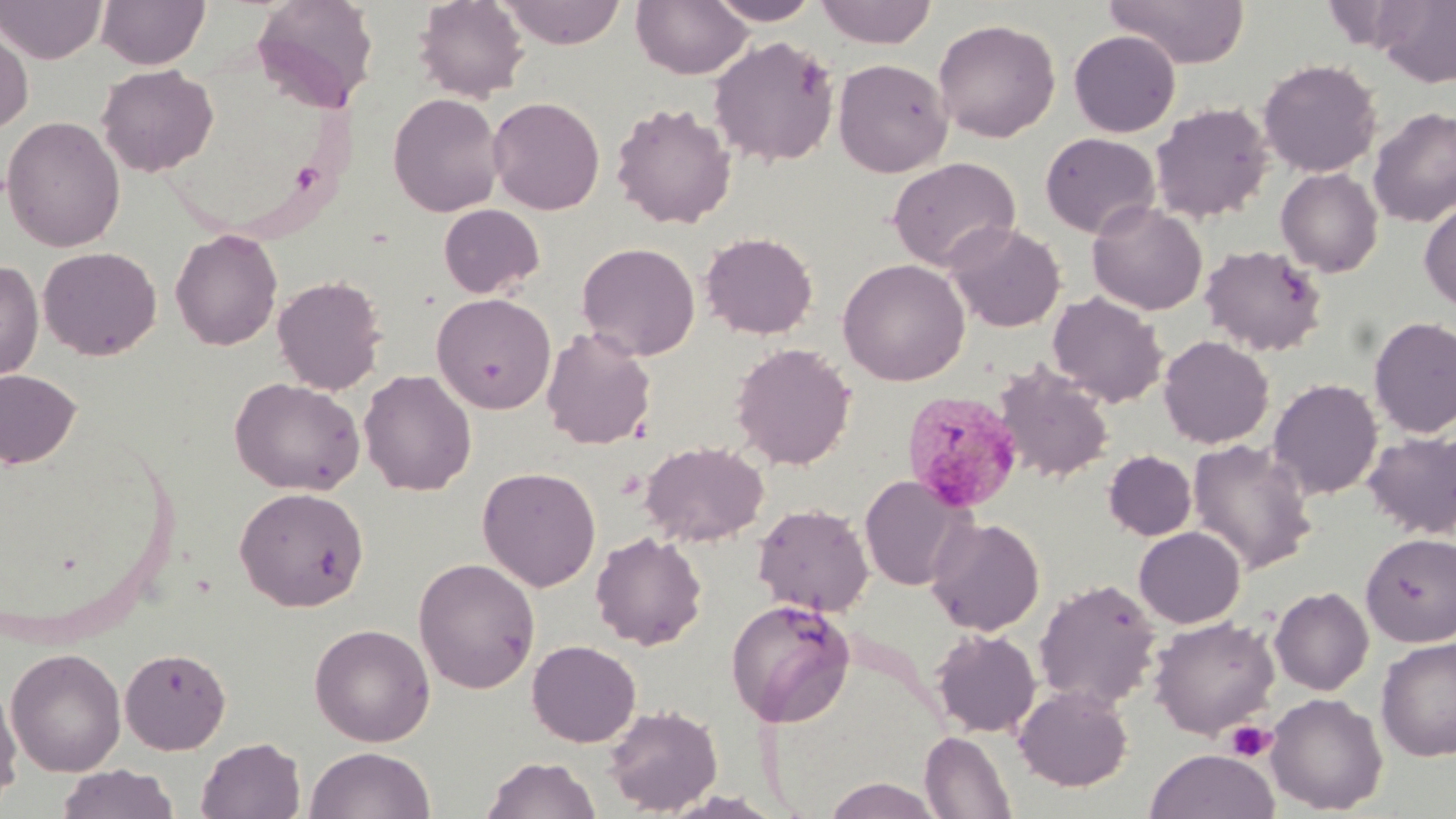
Summary:
  - Coordinate format: approximate bounding boxes as [x1, y1, x2, y2] in pixels
  - Uninfected red blood cell locations: [0, 0, 107, 64], [95, 0, 211, 69], [251, 0, 380, 113], [413, 0, 530, 102], [497, 0, 627, 48], [631, 0, 753, 79], [706, 0, 823, 25], [815, 0, 937, 48], [1103, 0, 1251, 68], [933, 18, 1060, 142], [0, 20, 35, 135], [1068, 30, 1181, 137], [708, 34, 840, 167], [833, 57, 953, 177], [1258, 58, 1381, 177], [96, 64, 219, 177], [387, 92, 505, 217], [487, 96, 605, 215], [610, 101, 737, 229], [1150, 101, 1273, 223], [1368, 106, 1456, 228], [1, 116, 126, 252], [1039, 132, 1160, 238], [887, 156, 1021, 272], [1276, 167, 1383, 277], [1419, 199, 1456, 313], [1087, 200, 1208, 315], [437, 203, 545, 299], [945, 222, 1066, 332], [170, 228, 283, 351], [700, 231, 818, 339], [576, 241, 700, 360], [1199, 243, 1328, 357], [38, 246, 162, 360], [837, 258, 971, 386], [0, 260, 44, 383], [271, 274, 388, 395], [1047, 291, 1168, 408], [432, 292, 556, 414], [1369, 316, 1456, 439], [541, 327, 657, 450], [1158, 335, 1274, 449], [731, 342, 856, 470], [993, 362, 1114, 483], [0, 368, 81, 470], [358, 369, 477, 496], [230, 377, 366, 496], [1268, 378, 1383, 499], [1363, 430, 1456, 539], [1186, 438, 1319, 575], [640, 441, 769, 547], [1103, 450, 1197, 540], [477, 465, 601, 591], [858, 475, 971, 591], [234, 486, 369, 611], [753, 503, 874, 617], [927, 516, 1045, 636], [1133, 526, 1245, 628], [590, 531, 708, 650], [1361, 533, 1456, 646], [412, 557, 541, 694], [1033, 578, 1161, 710], [1269, 585, 1374, 695], [725, 598, 855, 726], [1149, 615, 1279, 739], [309, 623, 436, 746], [931, 627, 1041, 737], [1376, 636, 1456, 761], [527, 639, 641, 747], [119, 646, 231, 754], [5, 647, 126, 777], [0, 679, 22, 809], [1013, 684, 1134, 791], [1266, 692, 1388, 813], [603, 703, 723, 816], [920, 731, 1017, 819], [196, 736, 306, 819], [304, 746, 435, 819], [1144, 748, 1279, 819], [481, 755, 600, 819], [56, 764, 180, 819], [822, 778, 944, 818]
  - Plasmodium malariae-infected red blood cell locations: [902, 389, 1024, 512]
  - Platelet locations: [1224, 720, 1276, 762]
  - Slide-level diagnosis: Plasmodium malariae
  - Preparation: thin blood smear
  - Field of view: one of a larger specimen
  - Modality: light microscopy
  - Stain: May-Grünwald-Giemsa
  - Magnification: 1000x
  - Image size: 1456×819 pixels